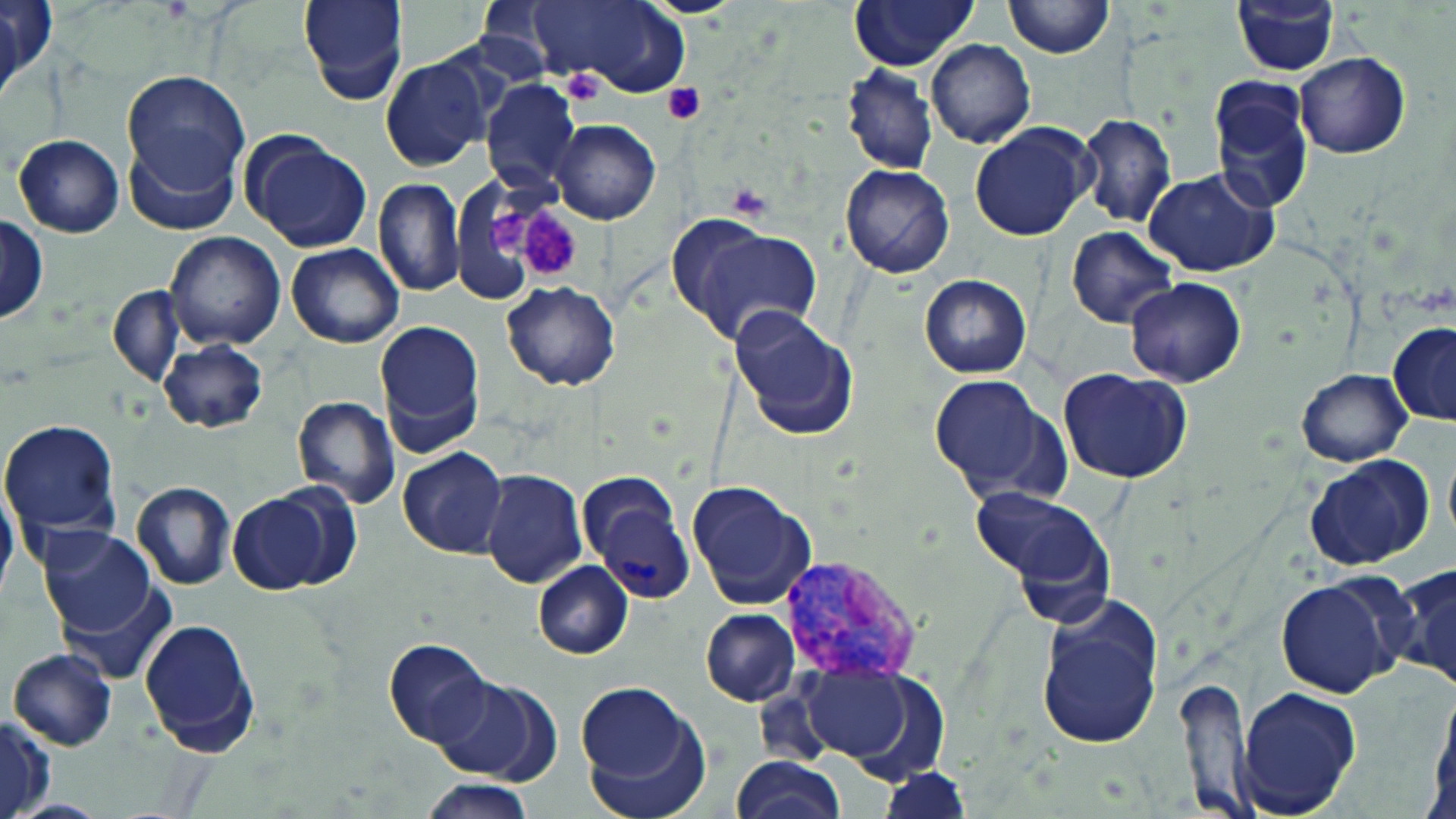
slide-level diagnosis = Plasmodium vivax
uninfected red blood cell locations = approximate bounding boxes as named x1/y1/x2/y2 corners in pixels: (x1=298, y1=0, x2=407, y2=104), (x1=849, y1=0, x2=977, y2=70), (x1=1005, y1=0, x2=1113, y2=58), (x1=0, y1=1, x2=54, y2=93), (x1=530, y1=1, x2=690, y2=96), (x1=1232, y1=2, x2=1339, y2=75), (x1=0, y1=4, x2=27, y2=108), (x1=926, y1=40, x2=1034, y2=149), (x1=1294, y1=53, x2=1409, y2=159), (x1=380, y1=56, x2=492, y2=173), (x1=841, y1=65, x2=938, y2=176), (x1=120, y1=71, x2=251, y2=195), (x1=480, y1=79, x2=581, y2=193), (x1=1207, y1=80, x2=1314, y2=216), (x1=1076, y1=114, x2=1177, y2=228), (x1=551, y1=120, x2=659, y2=225), (x1=968, y1=123, x2=1097, y2=241), (x1=242, y1=132, x2=371, y2=252), (x1=13, y1=135, x2=123, y2=237), (x1=123, y1=136, x2=240, y2=236), (x1=839, y1=164, x2=956, y2=278), (x1=1143, y1=168, x2=1279, y2=277), (x1=372, y1=179, x2=467, y2=296), (x1=0, y1=216, x2=47, y2=323), (x1=666, y1=216, x2=821, y2=347), (x1=1066, y1=226, x2=1178, y2=329), (x1=164, y1=231, x2=286, y2=351), (x1=286, y1=243, x2=405, y2=348), (x1=919, y1=274, x2=1031, y2=378), (x1=1124, y1=277, x2=1249, y2=387), (x1=500, y1=281, x2=621, y2=391), (x1=107, y1=283, x2=185, y2=387), (x1=727, y1=304, x2=858, y2=441), (x1=374, y1=319, x2=485, y2=450), (x1=1388, y1=323, x2=1456, y2=426), (x1=158, y1=339, x2=266, y2=433), (x1=1058, y1=368, x2=1192, y2=484), (x1=1295, y1=369, x2=1412, y2=466), (x1=927, y1=374, x2=1059, y2=499), (x1=291, y1=397, x2=400, y2=508), (x1=2, y1=420, x2=123, y2=537), (x1=1443, y1=440, x2=1456, y2=553), (x1=397, y1=448, x2=508, y2=559), (x1=1303, y1=456, x2=1436, y2=572), (x1=576, y1=466, x2=680, y2=563), (x1=480, y1=469, x2=587, y2=589), (x1=687, y1=479, x2=817, y2=611), (x1=0, y1=482, x2=18, y2=604), (x1=132, y1=482, x2=235, y2=589), (x1=225, y1=488, x2=355, y2=596), (x1=973, y1=488, x2=1116, y2=612), (x1=36, y1=526, x2=160, y2=642), (x1=533, y1=561, x2=633, y2=658), (x1=1394, y1=563, x2=1456, y2=691), (x1=61, y1=574, x2=175, y2=683), (x1=1273, y1=576, x2=1408, y2=700), (x1=1034, y1=594, x2=1165, y2=752), (x1=700, y1=608, x2=801, y2=706), (x1=139, y1=618, x2=261, y2=756), (x1=383, y1=638, x2=494, y2=747), (x1=7, y1=648, x2=116, y2=751), (x1=798, y1=663, x2=947, y2=779), (x1=430, y1=673, x2=559, y2=783), (x1=1175, y1=674, x2=1257, y2=818), (x1=1235, y1=685, x2=1361, y2=817), (x1=1428, y1=685, x2=1456, y2=812), (x1=573, y1=686, x2=711, y2=819), (x1=0, y1=715, x2=50, y2=819), (x1=730, y1=755, x2=845, y2=818), (x1=879, y1=768, x2=970, y2=817), (x1=415, y1=777, x2=539, y2=818)
preparation = thin blood smear
field of view = single
stain = May-Grünwald-Giemsa
Plasmodium vivax-infected red blood cell locations = approximate bounding boxes as named x1/y1/x2/y2 corners in pixels: (x1=595, y1=503, x2=693, y2=602), (x1=780, y1=557, x2=920, y2=680)
platelet locations = approximate bounding boxes as named x1/y1/x2/y2 corners in pixels: (x1=561, y1=72, x2=609, y2=107), (x1=663, y1=83, x2=706, y2=124), (x1=726, y1=182, x2=775, y2=221), (x1=518, y1=205, x2=582, y2=281), (x1=490, y1=207, x2=533, y2=250)
magnification = 1000x
image size = 1456×819 pixels
modality = optical microscopy